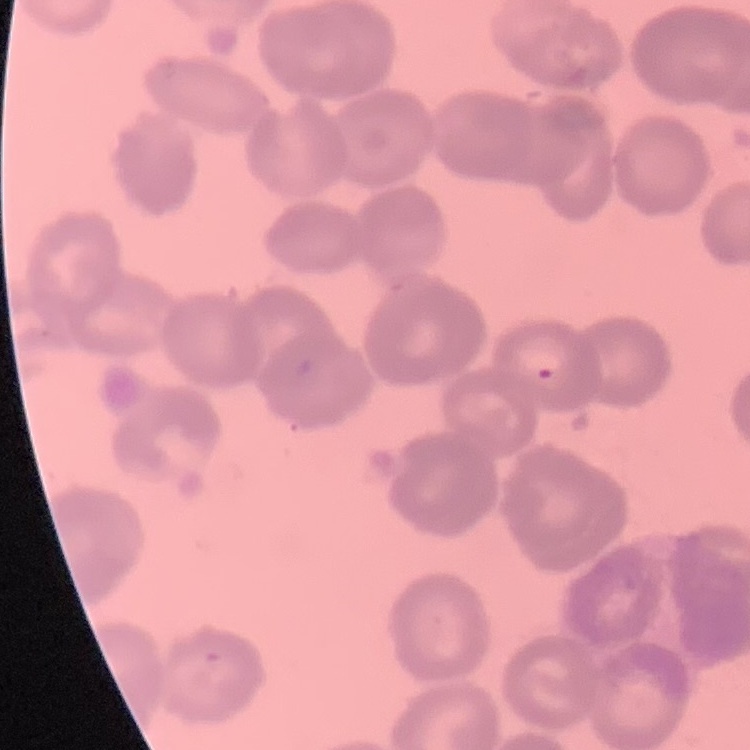

Summary:
  - Erythrocyte morphology: rouleaux formation
  - Stain: Field's or Giemsa
  - Image type: square crop of a larger photomicrograph
  - Preparation: thin peripheral smear